Name the parasite shown.
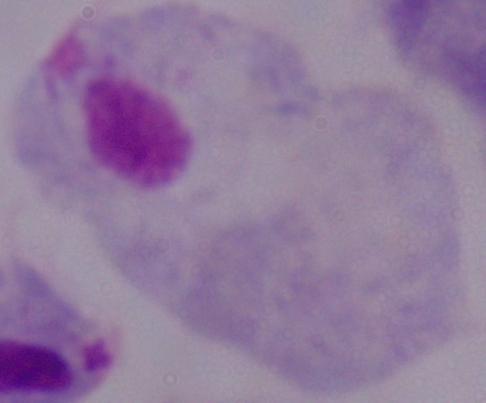
A trichomonad.

Summary:
  - Modality: photomicrograph
  - Magnification: 1000x